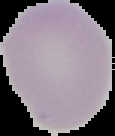
image type = segmented cell region with the area outside set to black
preparation = thin blood film
image size = 115×136 pixels
result = negative for malaria parasites